Assess this cell for malaria.
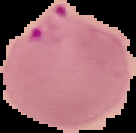

It is parasitized.

Cell region segmented out of the field of view; the surrounding area is masked to black. Image is 136×133 pixels. From a thin blood smear.